Outline each Plasmodium malariae-infected red blood cell.
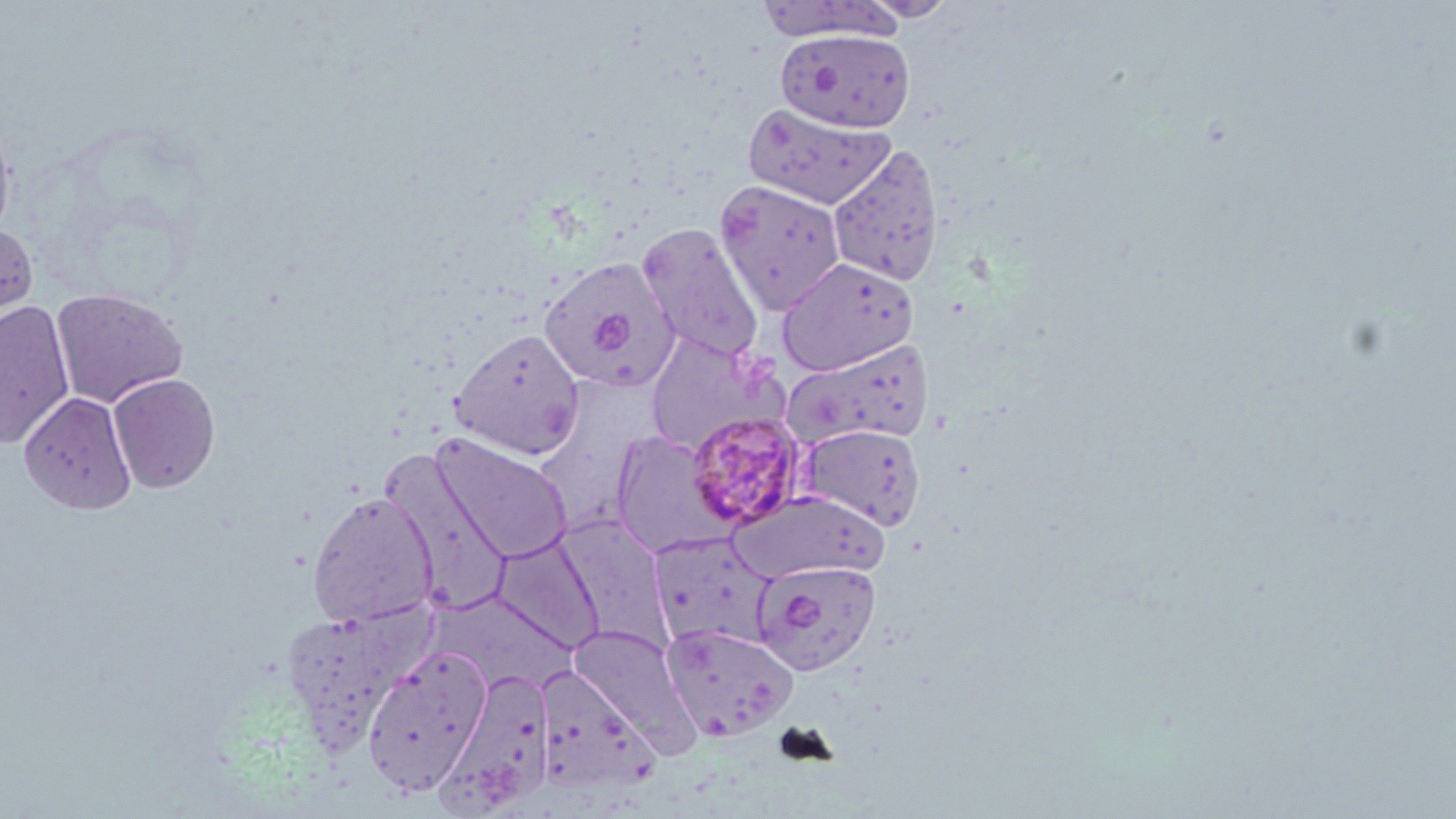
Approximate bounding boxes as [x1, y1, x2, y2] in pixels.
Plasmodium malariae-infected red blood cells: [685, 409, 808, 530].

slide_level_diagnosis: Plasmodium malariae
preparation: thin blood smear
image_size: 1456×819 pixels
uninfected_red_blood_cell_locations: 'approximate bounding boxes as [x1, y1, x2, y2] in pixels: [862, 0, 958, 21], [777, 29, 916, 133], [743, 102, 895, 210], [0, 112, 16, 248], [828, 142, 946, 287], [715, 179, 847, 315], [636, 222, 765, 365], [0, 223, 38, 328], [538, 256, 680, 393], [777, 257, 919, 376], [51, 287, 188, 408], [0, 301, 75, 448], [450, 328, 586, 460], [643, 331, 786, 456], [780, 338, 933, 450], [107, 373, 221, 493], [20, 392, 137, 514], [797, 423, 926, 530], [611, 430, 732, 558], [431, 434, 574, 564], [381, 448, 514, 615], [729, 490, 888, 583], [307, 491, 439, 627], [648, 529, 779, 650], [492, 533, 603, 654], [750, 558, 882, 676], [279, 603, 436, 752], [660, 621, 799, 742], [569, 623, 695, 747], [361, 646, 492, 795], [436, 665, 559, 816], [533, 666, 656, 798]'
stain: May-Grünwald-Giemsa
modality: optical microscopy
field_of_view: single
magnification: 1000x